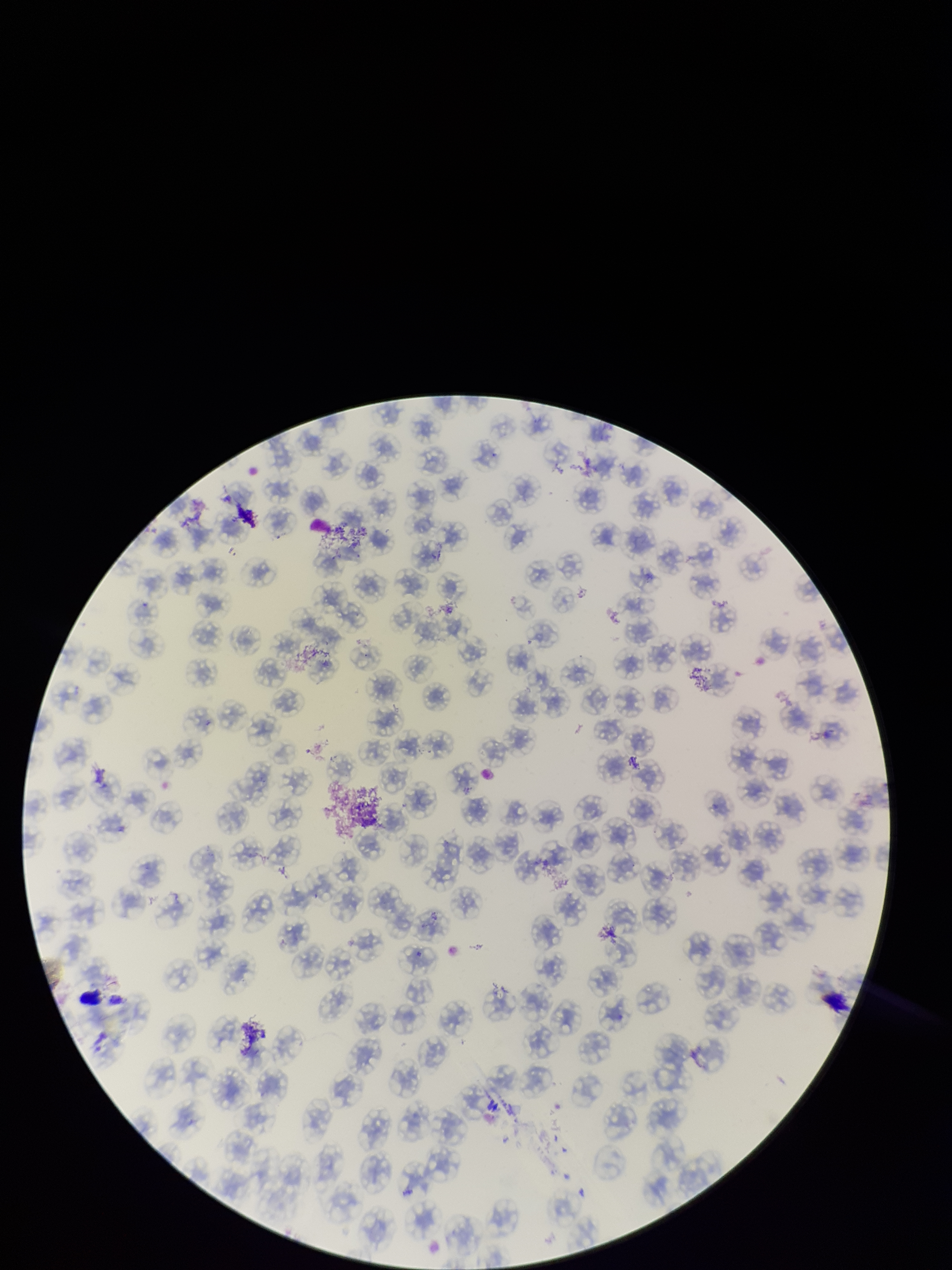
{
  "parasitized_red_blood_cell_count": 0,
  "field_of_view": "one from this slide",
  "patient_malaria_status": "negative",
  "preparation": "thin blood smear",
  "capture": "smartphone photograph through the microscope eyepiece",
  "parasitized_red_blood_cells": "none identified",
  "stain": "Giemsa",
  "image_size": "952×1270 pixels",
  "red_blood_cell_count": 120
}